Assess this cell for malaria.
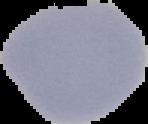

It is uninfected.

image size = 148×124 pixels
image type = segmented cell region with the area outside set to black
preparation = thin blood smear